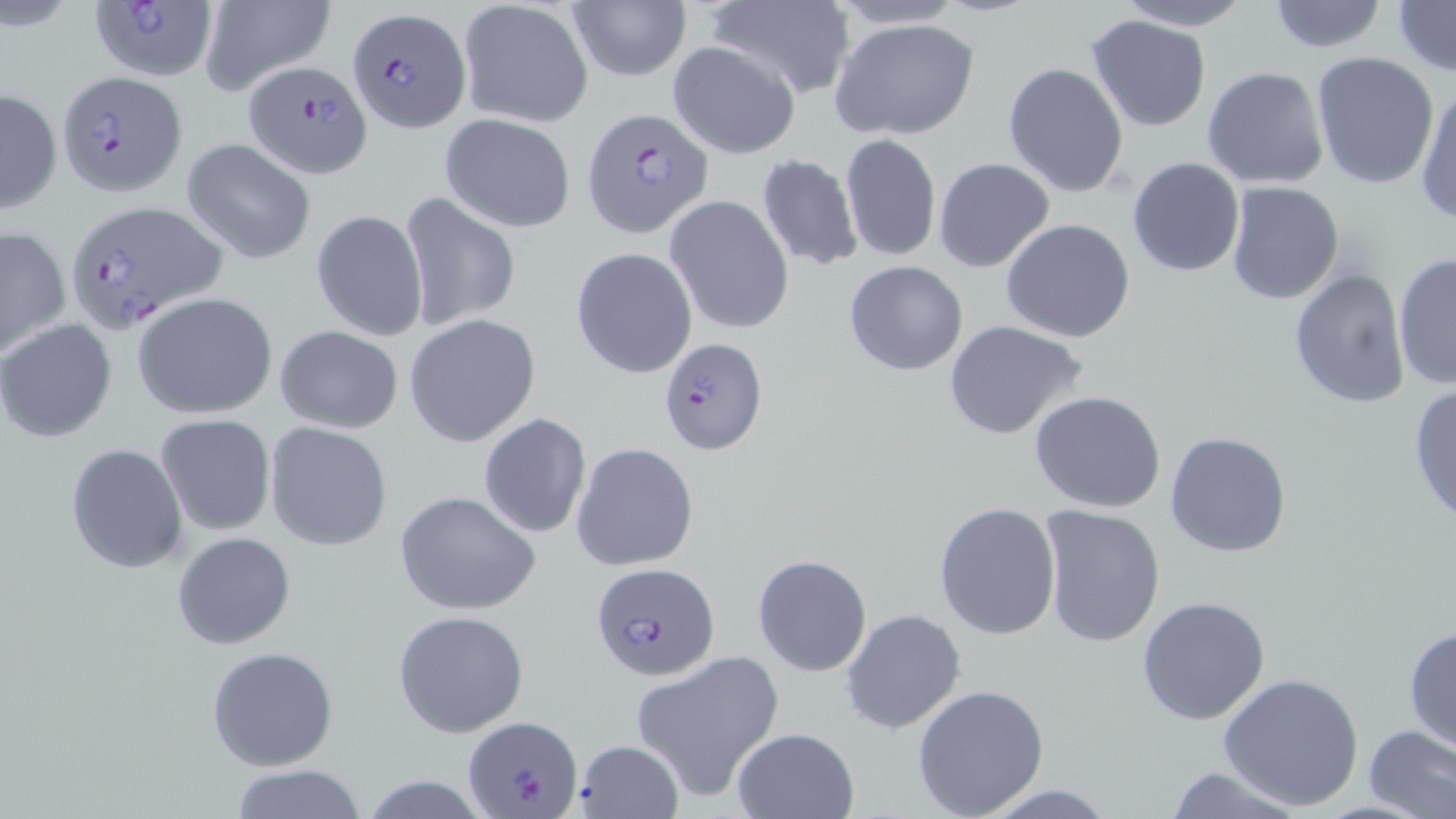

Summary:
  - Coordinate format: approximate bounding boxes as (x1, y1, x2, y2) in pixels
  - Uninfected red blood cell locations: (197, 0, 337, 97), (701, 0, 856, 99), (825, 0, 971, 30), (1113, 0, 1257, 31), (1262, 0, 1391, 53), (457, 1, 594, 129), (1393, 1, 1455, 76), (567, 2, 691, 82), (1086, 13, 1214, 132), (829, 16, 979, 141), (666, 41, 800, 160), (1310, 52, 1440, 191), (1002, 61, 1130, 197), (1202, 66, 1330, 189), (1413, 83, 1456, 227), (1, 87, 62, 213), (439, 113, 577, 233), (840, 132, 942, 263), (181, 137, 317, 264), (756, 155, 865, 272), (1127, 156, 1246, 276), (934, 157, 1054, 271), (1225, 181, 1345, 303), (400, 191, 522, 332), (664, 196, 794, 334), (310, 208, 430, 343), (1001, 218, 1135, 341), (0, 226, 71, 357), (570, 247, 698, 378), (1393, 251, 1456, 392), (844, 260, 968, 376), (1287, 269, 1412, 410), (133, 292, 276, 418), (405, 314, 542, 449), (0, 319, 117, 442), (943, 319, 1092, 441), (274, 325, 404, 434), (1409, 382, 1456, 528), (1028, 390, 1169, 515), (154, 413, 276, 538), (477, 414, 592, 538), (265, 422, 394, 552), (1165, 430, 1291, 557), (65, 442, 190, 576), (571, 442, 699, 572), (394, 489, 541, 615), (934, 501, 1061, 639), (1038, 506, 1166, 650), (171, 531, 296, 649), (752, 554, 872, 675), (1137, 596, 1271, 725), (840, 608, 968, 735), (392, 609, 531, 737), (1404, 624, 1456, 759), (206, 645, 338, 771), (634, 651, 783, 801), (1219, 672, 1364, 811), (911, 683, 1050, 818), (1362, 724, 1456, 819), (731, 727, 859, 819), (574, 738, 684, 818), (228, 764, 368, 819), (1161, 765, 1306, 818), (358, 776, 492, 817), (972, 781, 1121, 818)
  - Plasmodium falciparum-infected red blood cell locations: (89, 1, 217, 83), (348, 9, 470, 133), (244, 60, 373, 176), (53, 69, 185, 199), (583, 109, 713, 238), (61, 200, 227, 331), (660, 337, 767, 455), (590, 561, 722, 684), (464, 713, 584, 817)
  - Slide-level diagnosis: Plasmodium falciparum
  - Field of view: single
  - Magnification: 1000x
  - Image size: 1456×819 pixels
  - Modality: optical microscopy
  - Stain: May-Grünwald-Giemsa
  - Preparation: thin blood smear